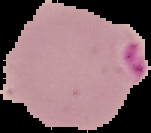

Summary:
  - Image type: segmented cell region on a black background
  - Malaria status: parasitized
  - Preparation: thin blood smear
  - Image size: 151×133 pixels